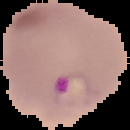
Result: malaria parasites identified. The area outside the segmented cell region is set to black. From a thin blood film. Image is 130×130 pixels.